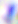 Photomicrograph. Toxoplasma gondii is shown. 400x magnification.